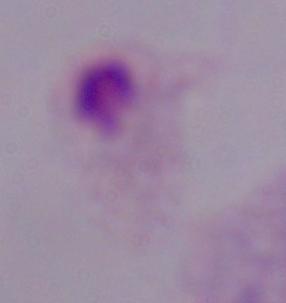
modality: micrograph
identification: trichomonad
magnification: 1000x